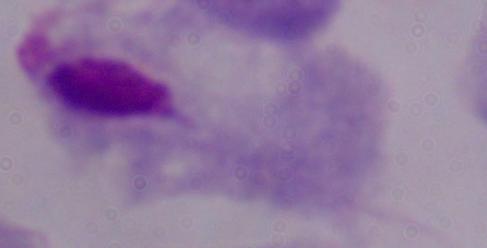
Summary:
  - Identification: trichomonad
  - Magnification: 1000x
  - Modality: photomicrograph